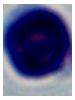

magnification = 1000x
identification = white blood cell
modality = photomicrograph